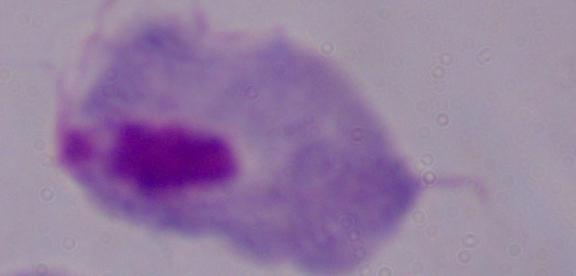

A trichomonad is shown. Micrograph. Captured at 1000x magnification.